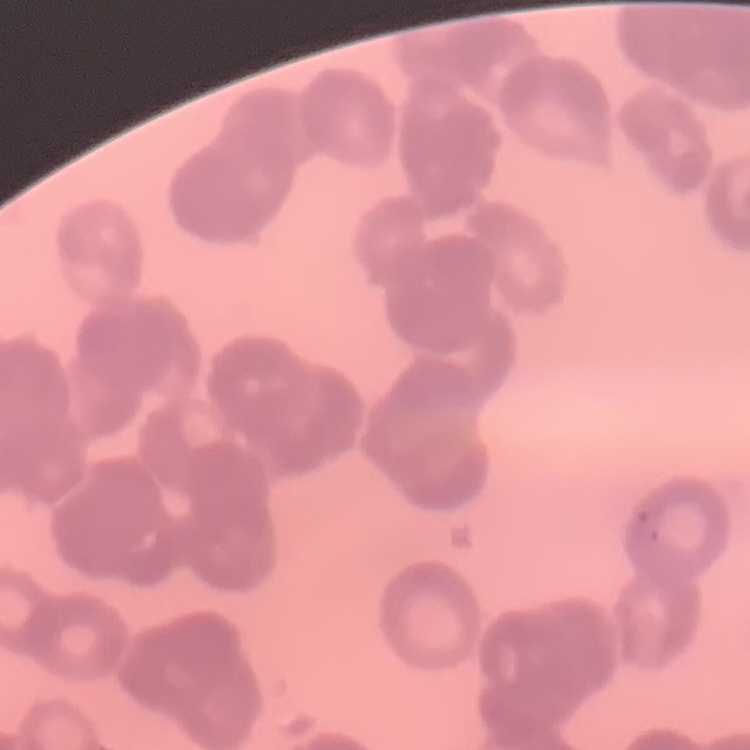 The red blood cells exhibit rouleaux formation. Thin blood film. Stained with either Field's or Giemsa. One tile cut from a larger photomicrograph.